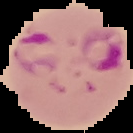

From a thin blood smear. Result: malaria parasites detected. Cell region segmented out of the field of view; the surrounding area is masked to black. Image is 133×133 pixels.